Identify the cell.
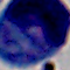

This is a leukocyte.

{
  "modality": "photomicrograph",
  "magnification": "1000x"
}